Assess this cell for malaria.
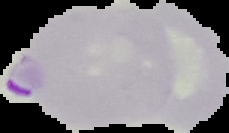
Parasitized.

{
  "image_size": "229×133 pixels",
  "preparation": "thin blood film",
  "image_type": "cell region segmented out of the field of view; surrounding area masked to black"
}